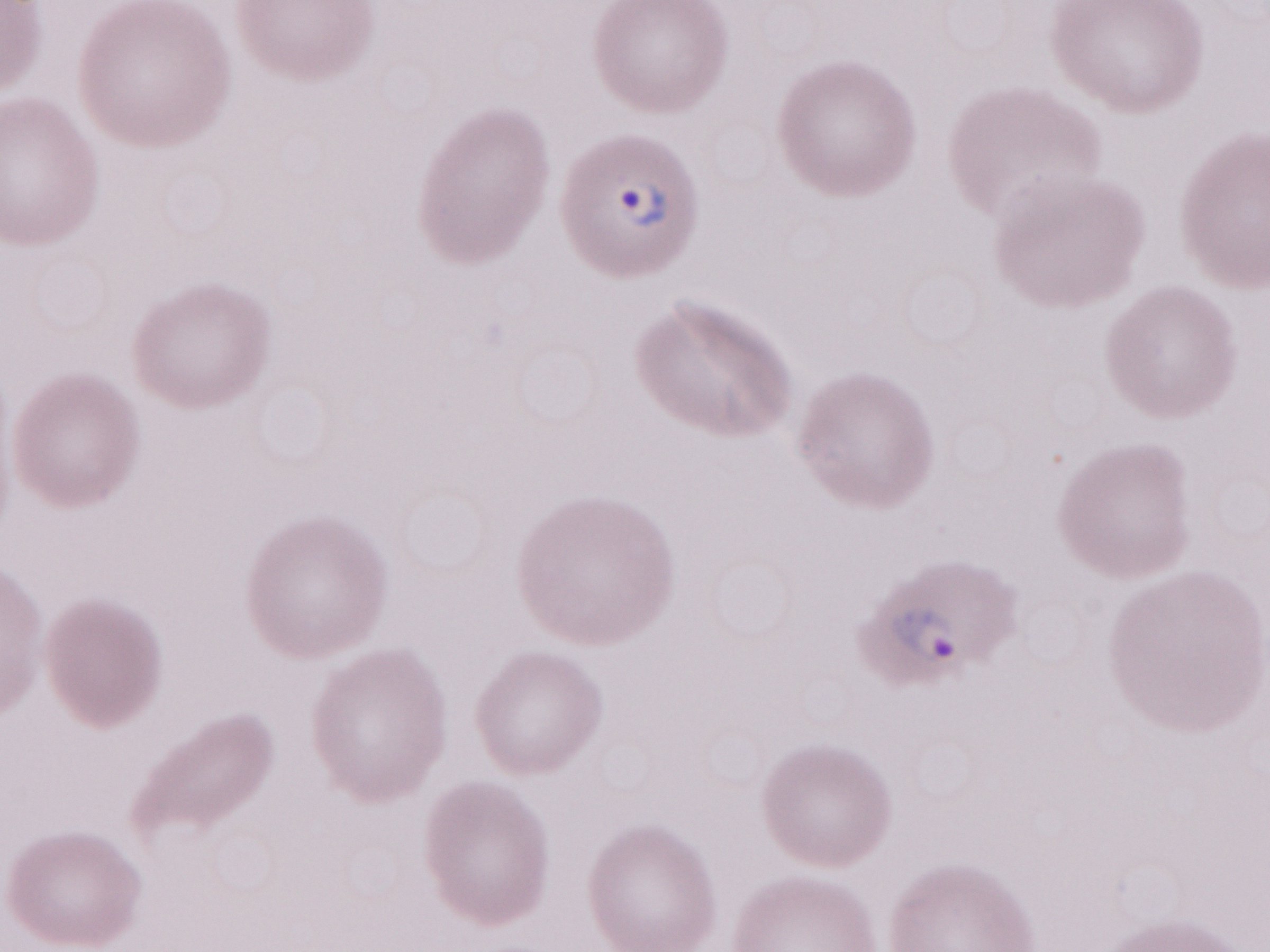
Single field of view. May-Grünwald-Giemsa (MGG) stain. Patient diagnosis: malaria infection. Olympus BX43 microscope and DP73 digital camera. Thin blood smear. Image is 1270×952 pixels. Magnification: 1,000x.